Classify this cell by malaria status.
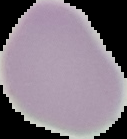
Uninfected.

Image is 127×139 pixels. Segmented cell region on a black background. From a thin blood film.